Locate and identify every blood parasite.
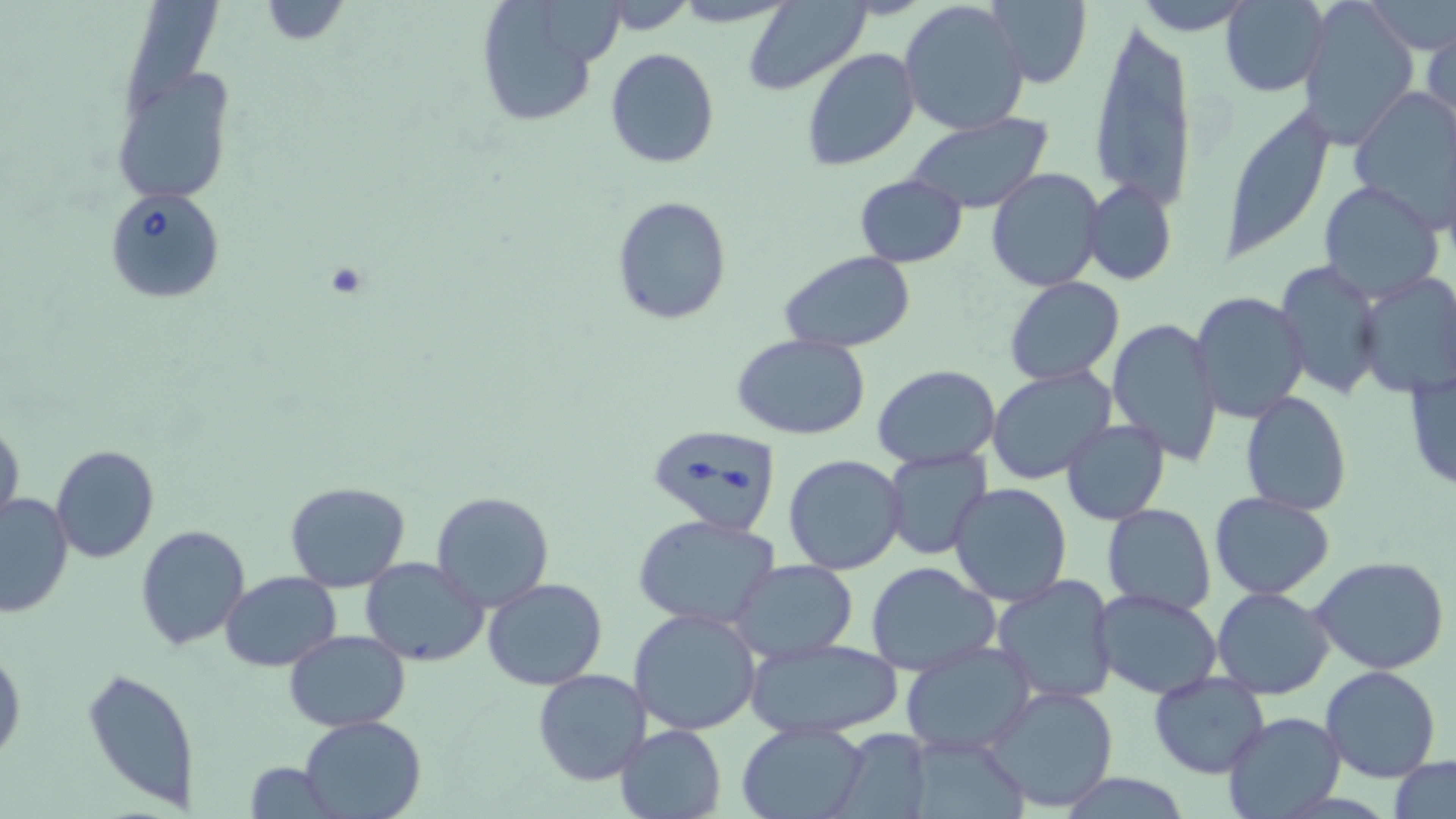

Approximate bounding boxes as [x1, y1, x2, y2] in pixels.
Babesia divergens-infected red blood cells: [107, 188, 225, 302], [646, 423, 782, 537].
No Plasmodium falciparum, Plasmodium ovale, Plasmodium malariae, Plasmodium vivax, or Trypanosoma brucei observed.

slide_level_diagnosis: Babesia divergens
magnification: 1000x
uninfected_red_blood_cell_locations: 'approximate bounding boxes as [x1, y1, x2, y2] in pixels: [257, 0, 353, 45], [742, 0, 875, 96], [899, 0, 1031, 137], [986, 0, 1092, 88], [1133, 0, 1253, 32], [1298, 0, 1420, 147], [1368, 0, 1455, 54], [473, 1, 608, 129], [543, 1, 625, 67], [1220, 1, 1328, 97], [117, 2, 224, 120], [1086, 19, 1200, 214], [1423, 21, 1455, 132], [801, 46, 920, 171], [605, 48, 720, 168], [111, 70, 232, 205], [1348, 88, 1456, 227], [1219, 108, 1334, 263], [903, 114, 1055, 215], [987, 167, 1106, 294], [853, 174, 968, 268], [1317, 180, 1444, 302], [1082, 181, 1176, 286], [611, 197, 732, 324], [781, 251, 917, 353], [1276, 260, 1386, 401], [1357, 272, 1456, 397], [1004, 275, 1125, 385], [1190, 292, 1310, 426], [1106, 316, 1224, 466], [730, 332, 871, 440], [1404, 363, 1454, 494], [873, 364, 1001, 468], [986, 365, 1117, 487], [1239, 390, 1354, 517], [1060, 417, 1171, 526], [0, 419, 24, 535], [50, 445, 159, 564], [882, 447, 994, 562], [783, 453, 908, 574], [285, 481, 411, 593], [948, 482, 1073, 606], [430, 490, 557, 611], [1208, 492, 1335, 600], [0, 494, 73, 618], [1102, 503, 1217, 616], [633, 514, 781, 631], [135, 524, 250, 650], [359, 557, 489, 668], [1312, 558, 1451, 675], [730, 561, 859, 663], [866, 561, 1001, 676], [221, 570, 341, 672], [991, 574, 1118, 705], [481, 578, 609, 691], [1210, 587, 1336, 700], [1092, 588, 1223, 698], [629, 608, 763, 736], [285, 630, 410, 732], [746, 638, 904, 739], [898, 639, 1039, 756], [0, 645, 24, 769], [1319, 666, 1442, 783], [82, 667, 200, 810], [532, 667, 651, 786], [1148, 672, 1271, 778], [982, 684, 1119, 814], [1222, 710, 1346, 818], [299, 715, 426, 819], [736, 719, 872, 819], [614, 724, 726, 819], [829, 731, 935, 818], [1391, 755, 1455, 819], [243, 763, 338, 817]'
modality: light microscopy
preparation: thin blood smear
image_size: 1456×819 pixels
stain: May-Grünwald-Giemsa
field_of_view: one of a larger specimen